Assess this cell for malaria.
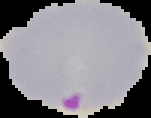
Parasitized.

From a thin blood smear. Segmented cell region on a black background. Image is 151×118 pixels.